Identify the malaria species.
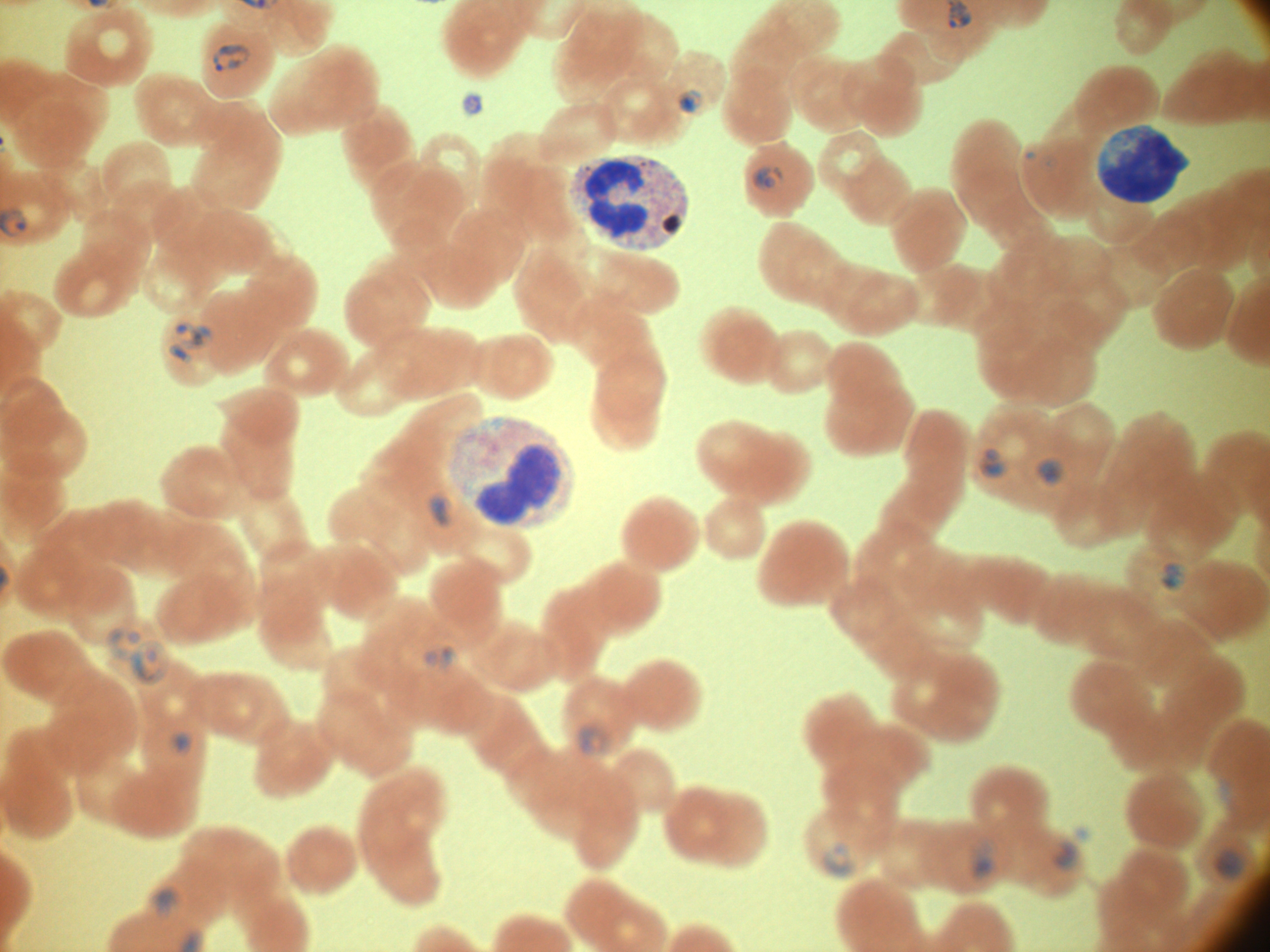

Plasmodium falciparum.

field of view = one from this slide
ring form locations = approximate bounding boxes as named x1/y1/x2/y2 corners in pixels, from the source annotation, which is not necessarily exhaustive: (x1=211, y1=43, x2=251, y2=73), (x1=678, y1=88, x2=706, y2=113), (x1=751, y1=166, x2=785, y2=192), (x1=171, y1=321, x2=215, y2=351), (x1=168, y1=341, x2=192, y2=365), (x1=979, y1=447, x2=1009, y2=478), (x1=1035, y1=459, x2=1066, y2=485), (x1=427, y1=491, x2=462, y2=529), (x1=1158, y1=562, x2=1189, y2=592), (x1=106, y1=627, x2=144, y2=661), (x1=129, y1=639, x2=171, y2=686), (x1=420, y1=645, x2=458, y2=673), (x1=578, y1=720, x2=613, y2=758), (x1=172, y1=731, x2=193, y2=756), (x1=1051, y1=839, x2=1080, y2=872), (x1=969, y1=840, x2=999, y2=881), (x1=820, y1=841, x2=855, y2=881), (x1=1215, y1=848, x2=1244, y2=880), (x1=153, y1=888, x2=180, y2=918)
microscope = Leica DM2000 with built-in camera
stain = Giemsa
image size = 1270×952 pixels
magnification = 100x
preparation = thin blood smear